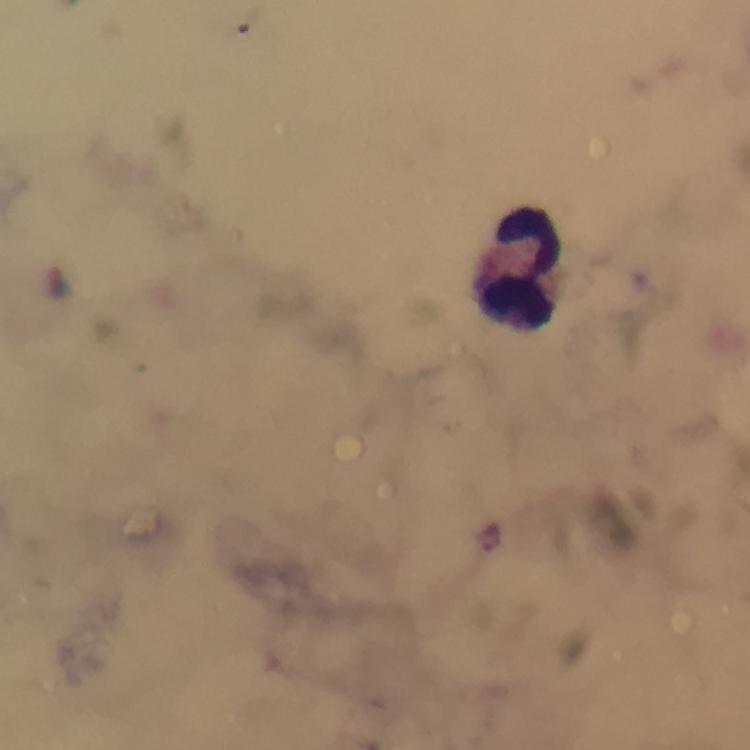
Approximate centers as {x, y} in pixels.
Summary:
  - Leukocyte locations: {519, 266}
  - Malaria parasite locations: {490, 538}
  - Magnification: 100x
  - Capture: smartphone photograph through a microscope
  - Preparation: thick blood film
  - Context: from a diagnostic examination for malaria
  - Cropped from: one field of view
  - Stain: Giemsa
  - Immersion oil: used
  - Image size: 750×750 pixels